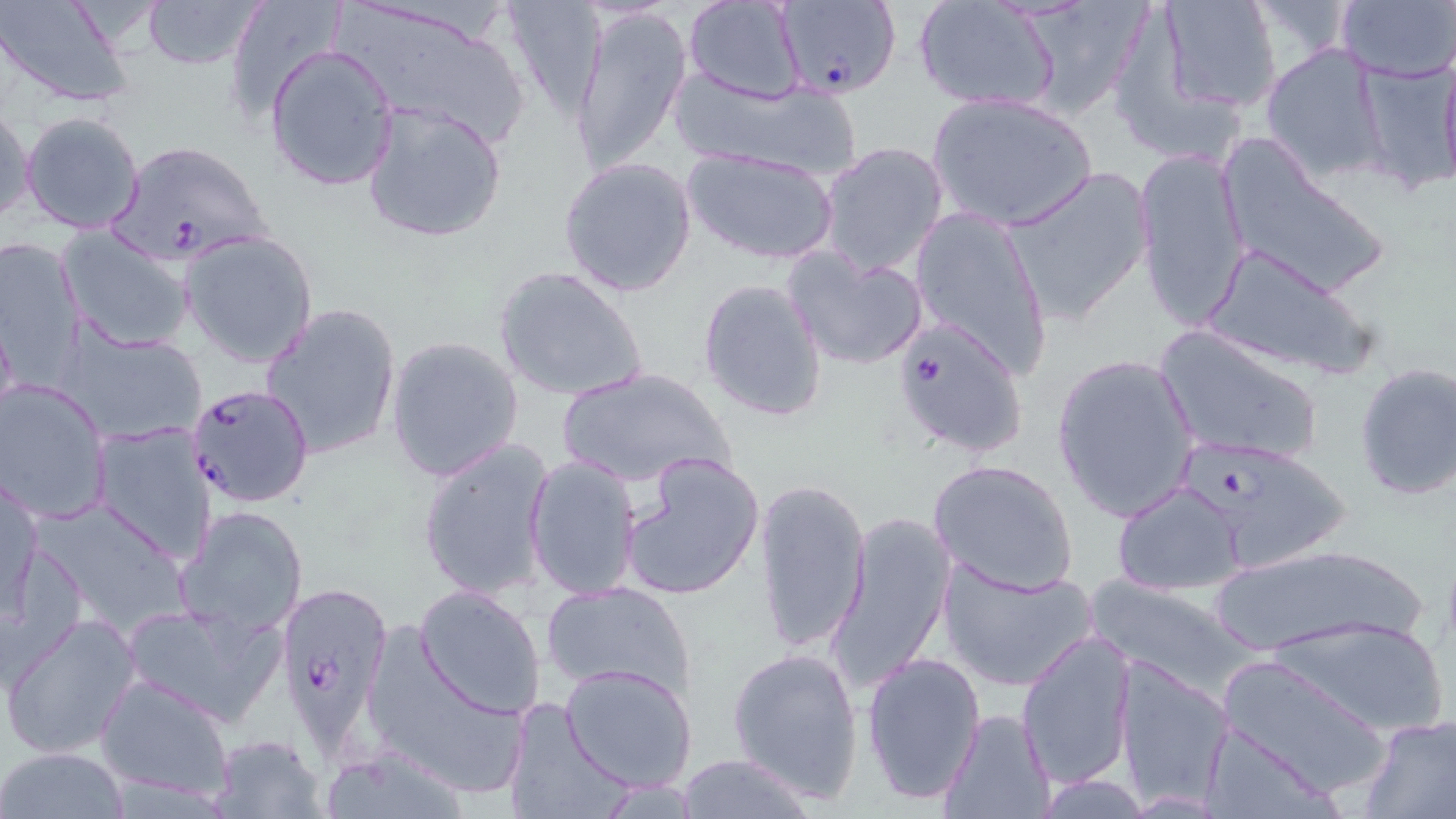

slide-level diagnosis = Plasmodium falciparum
uninfected red blood cell locations = approximate bounding boxes as (x1, y1, x2, y2) in pixels: (0, 0, 138, 109), (141, 0, 264, 72), (221, 0, 348, 124), (335, 0, 531, 144), (496, 0, 609, 120), (682, 0, 806, 105), (1018, 0, 1146, 119), (1157, 0, 1284, 114), (1333, 0, 1454, 84), (911, 1, 1063, 114), (568, 5, 693, 178), (265, 42, 399, 191), (1262, 43, 1393, 183), (1438, 50, 1456, 188), (1354, 55, 1455, 194), (672, 70, 861, 183), (925, 90, 1099, 233), (361, 99, 509, 245), (1, 101, 36, 226), (21, 111, 145, 233), (1219, 137, 1392, 301), (817, 140, 951, 276), (680, 145, 841, 266), (1133, 146, 1253, 331), (556, 156, 699, 299), (1001, 167, 1155, 325), (907, 206, 1055, 379), (55, 227, 196, 353), (179, 229, 319, 369), (0, 236, 89, 386), (1203, 246, 1379, 384), (784, 248, 929, 371), (493, 264, 651, 404), (696, 277, 828, 423), (262, 302, 402, 462), (1155, 323, 1324, 468), (59, 325, 206, 445), (384, 334, 524, 483), (1051, 351, 1201, 523), (1352, 361, 1456, 501), (556, 366, 733, 488), (1, 377, 112, 523), (90, 421, 218, 565), (416, 435, 555, 603), (619, 450, 766, 602), (524, 454, 642, 601), (926, 458, 1078, 595), (2, 473, 42, 617), (752, 475, 871, 658), (1112, 481, 1247, 596), (35, 495, 189, 636), (175, 504, 310, 636), (827, 511, 955, 693), (1217, 543, 1428, 654), (937, 560, 1097, 693), (540, 579, 698, 701), (1080, 579, 1260, 697), (413, 585, 547, 719), (123, 602, 283, 728), (3, 610, 143, 761), (1272, 616, 1449, 737), (1016, 628, 1137, 788), (363, 631, 532, 800), (727, 644, 865, 803), (860, 650, 984, 808), (1214, 656, 1395, 799), (1114, 659, 1234, 808), (559, 662, 698, 791), (96, 673, 236, 804), (950, 676, 1118, 811), (503, 698, 630, 819), (938, 708, 1055, 819), (1356, 714, 1456, 819), (1196, 719, 1335, 819), (210, 733, 328, 817), (315, 742, 474, 818), (1, 747, 128, 817), (673, 752, 818, 817), (1025, 774, 1160, 817)
modality = light microscopy
Plasmodium falciparum-infected red blood cell locations = approximate bounding boxes as (x1, y1, x2, y2) in pixels: (773, 0, 903, 102), (107, 139, 274, 267), (894, 317, 1028, 459), (183, 381, 314, 506), (1182, 438, 1357, 575), (278, 587, 393, 738)
image size = 1456×819 pixels
preparation = thin blood film
magnification = 1000x
field of view = one of a larger specimen
stain = May-Grünwald-Giemsa